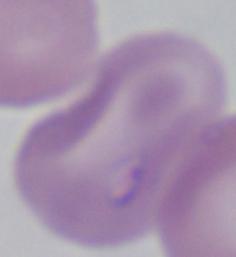

magnification: 1000x
modality: photomicrograph
identification: Babesia